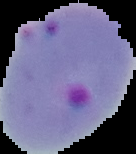

Summary:
  - Image size: 136×154 pixels
  - Preparation: thin blood film
  - Image type: cell region segmented out of the field of view; surrounding area masked to black
  - Result: Plasmodium parasites detected